Assess this cell for malaria.
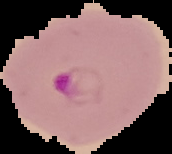

Parasitized.

Image is 172×154 pixels. Segmented cell region on a black background. From a thin blood film.